Give the extent of all Plasmodium vivax-infected red blood cells.
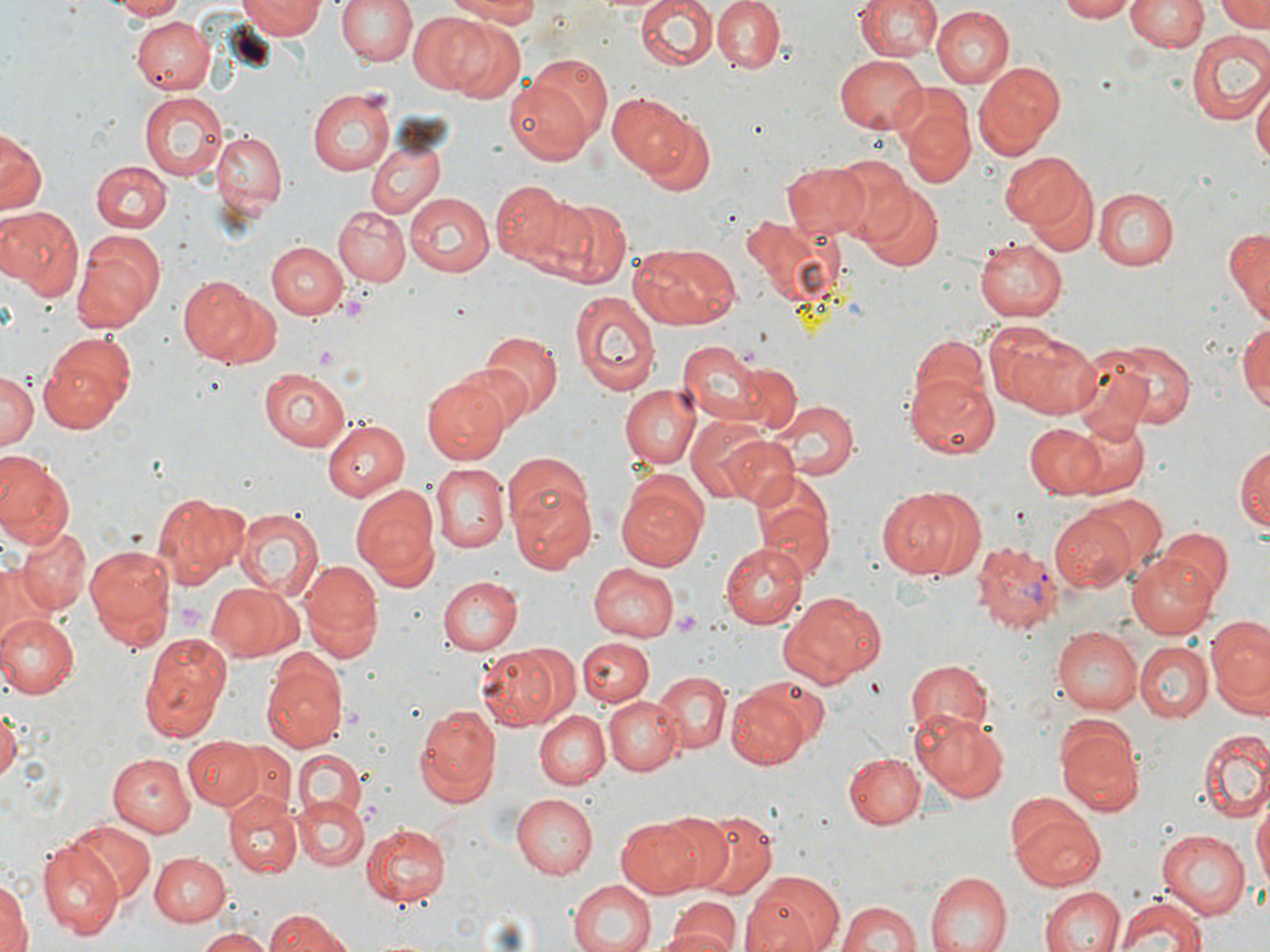
Approximate bounding boxes as (x1,y1)-(x2,y2) corner pairs in pixels.
Plasmodium vivax-infected red blood cells: (970,538)-(1065,637).

Uninfected red blood cell locations: (111,0)-(192,20), (238,0)-(323,40), (334,0)-(418,67), (447,0)-(546,25), (635,0)-(718,72), (711,0)-(785,73), (855,0)-(941,63), (1056,0)-(1134,22), (1126,0)-(1207,54), (1217,0)-(1268,33), (931,6)-(1014,87), (409,13)-(494,95), (133,16)-(211,94), (442,19)-(527,104), (1186,30)-(1270,126), (833,55)-(927,134), (975,62)-(1064,158), (503,77)-(596,167), (1253,82)-(1269,172), (308,89)-(394,175), (140,92)-(226,182), (609,92)-(689,175), (903,107)-(973,188), (641,114)-(715,196), (1,128)-(43,215), (209,129)-(286,216), (366,140)-(445,220), (998,149)-(1097,243), (830,157)-(915,242), (93,161)-(171,233), (782,161)-(873,240), (1029,175)-(1099,258), (488,178)-(580,275), (858,184)-(943,271), (1093,188)-(1179,271), (404,192)-(495,275), (551,198)-(629,290), (0,206)-(85,300), (334,207)-(410,286), (1225,226)-(1270,320), (72,229)-(167,332), (975,235)-(1067,320), (267,241)-(347,319), (629,242)-(742,328), (176,276)-(278,369), (571,291)-(660,398), (1237,319)-(1270,416), (1003,329)-(1104,419), (481,330)-(562,420), (39,333)-(136,431), (906,337)-(990,420), (675,338)-(771,425), (1104,341)-(1195,427), (1068,348)-(1151,429), (734,360)-(802,433), (0,369)-(39,455), (258,369)-(352,451), (902,370)-(999,458), (424,374)-(512,464), (618,384)-(701,468), (765,397)-(860,481), (684,417)-(775,501), (323,418)-(410,501), (1067,418)-(1150,496), (1023,424)-(1107,496), (712,431)-(800,507), (1235,442)-(1269,534), (0,454)-(74,550), (504,460)-(596,572), (429,461)-(509,553), (750,470)-(835,577), (614,473)-(709,571), (351,483)-(439,587), (878,485)-(974,580), (153,492)-(247,585), (1081,493)-(1167,573), (232,506)-(323,600), (1050,510)-(1140,593), (16,524)-(91,613), (1158,528)-(1235,607), (720,542)-(806,628), (84,543)-(175,650), (1126,552)-(1222,640), (299,560)-(383,662), (586,562)-(679,642), (1,565)-(41,648), (438,575)-(521,653), (207,582)-(303,662), (782,594)-(881,685), (0,613)-(77,699), (1207,616)-(1270,706), (1054,627)-(1143,713), (138,632)-(231,741), (579,638)-(650,706), (477,643)-(576,729), (1136,643)-(1211,721), (262,651)-(347,752), (902,657)-(994,742), (653,669)-(730,754), (724,683)-(818,770), (604,697)-(682,774), (0,701)-(20,787), (412,701)-(500,807), (912,709)-(1008,801), (536,711)-(611,788), (1058,722)-(1145,817), (1198,726)-(1270,822), (183,736)-(261,810), (223,742)-(295,822), (106,751)-(196,838), (295,751)-(365,820), (842,752)-(925,830), (223,792)-(302,878), (512,792)-(598,877), (294,798)-(367,870), (1254,802)-(1269,893), (1009,807)-(1107,891), (656,810)-(739,892), (692,810)-(778,898), (615,815)-(707,899), (70,821)-(153,902), (361,822)-(451,906), (1156,829)-(1250,919), (38,841)-(124,939), (149,853)-(233,928), (743,869)-(843,952), (928,872)-(1012,952), (0,874)-(30,952), (567,878)-(655,952), (1039,886)-(1124,952), (834,893)-(1000,952), (1115,894)-(1209,952), (665,901)-(740,952), (837,901)-(923,952), (266,911)-(356,952), (647,927)-(740,952), (191,928)-(275,952). Platelet locations: (341,290)-(372,320), (174,599)-(209,635), (674,610)-(699,634). Slide-level diagnosis: Plasmodium vivax. Thin blood film. Image is 1270×952 pixels. 1000x magnification. Single field of view. May-Grünwald-Giemsa-stained preparation. Optical microscopy.